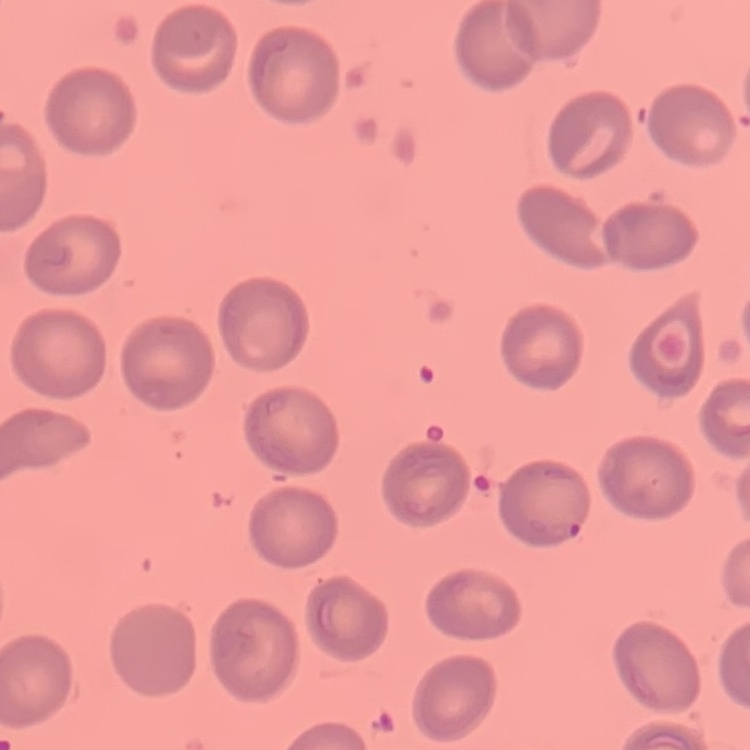 The erythrocytes exhibit no rouleaux formation. Thin blood smear. Field's or Giemsa stain. One tile cut from a larger photomicrograph.